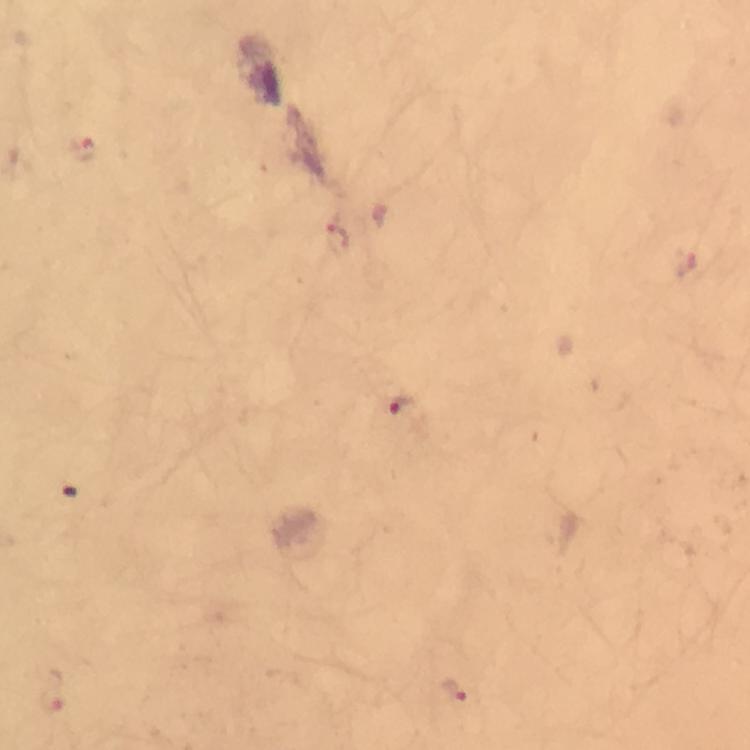

immersion oil = applied
image size = 750×750 pixels
malaria parasite locations = approximate centers as {x, y} in pixels: {85, 149}, {405, 411}, {456, 690}, {51, 701}
magnification = 100x
cropped from = a single field of view
capture = smartphone mounted on the microscope
context = from a diagnostic examination for malaria
preparation = thick blood film
stain = Giemsa